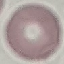 Result: negative for malaria parasites. Thin blood smear. Automatically extracted cell patch, resized to 64 × 64 pixels. Acquired by smartphone through the microscope eyepiece. Giemsa stain.